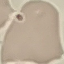

{
  "result": "no malaria parasites detected",
  "capture": "smartphone through the microscope eyepiece",
  "stain": "Giemsa",
  "preparation": "thin blood smear",
  "image_type": "automatically extracted cell patch, resized to 64 × 64 pixels"
}